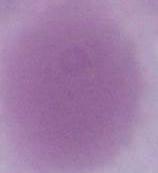

An erythrocyte is shown. Captured at 1000x magnification. Photomicrograph.